Comment on the morphology of the red blood cells.
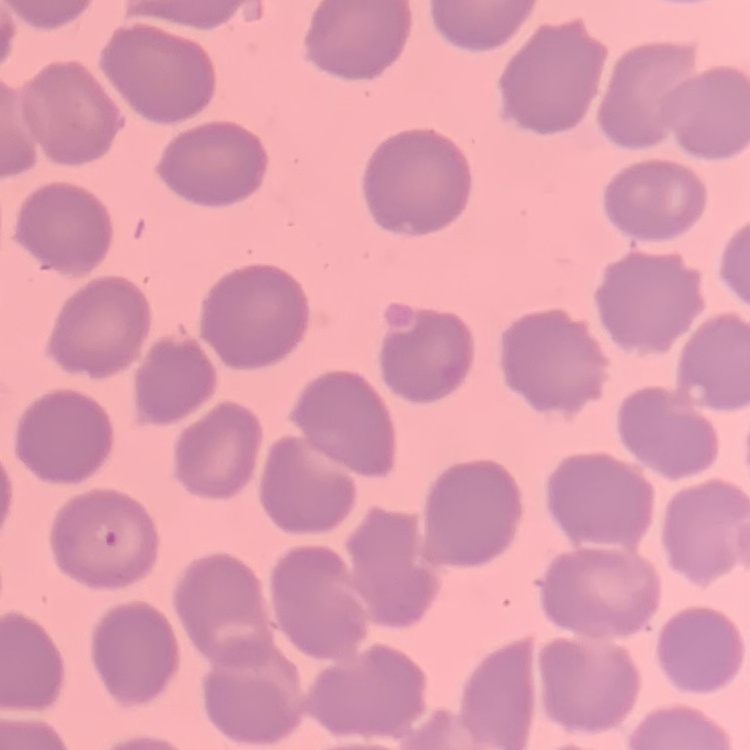
No rouleaux formation.

Field's or Giemsa stain. One tile cut from a larger photomicrograph. Thin peripheral smear.